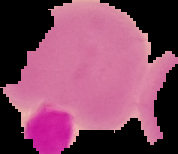

Segmented cell region on a black background. Result: negative for Plasmodium parasites. Image is 178×154 pixels. From a thin blood smear.